Point out Plasmodium parasites and leukocytes.
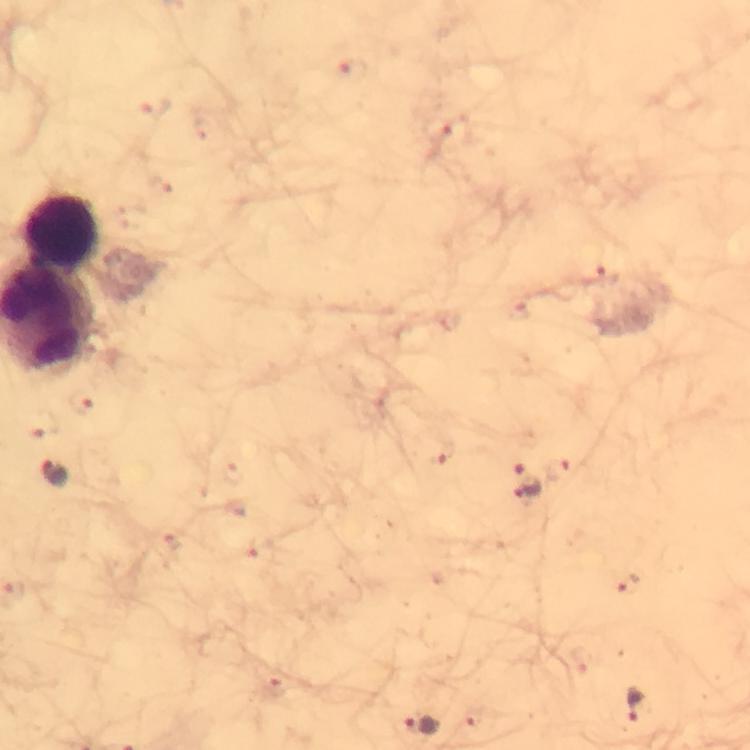

Approximate centers as [x, y] in pixels.
Plasmodium parasites: [601, 276], [55, 473], [527, 481], [626, 583], [639, 704], [420, 725].
Leukocytes: [64, 231].

image size = 750×750 pixels
context = from a malaria diagnostic workup
immersion oil = applied
capture = smartphone camera through the microscope
magnification = 100x
cropped from = a single field of view
stain = Giemsa
preparation = thick blood smear